State which parasite is depicted.
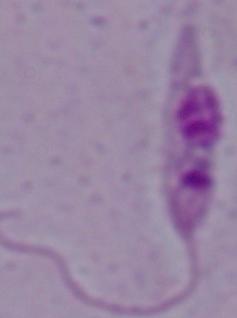

Leishmania.

Captured at 1000x magnification. Micrograph.